Name the parasite shown.
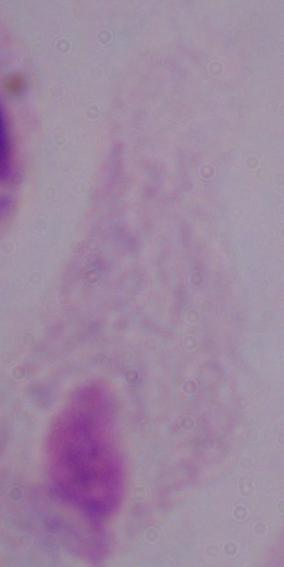

This is a trichomonad.

Summary:
  - Modality: micrograph
  - Magnification: 1000x